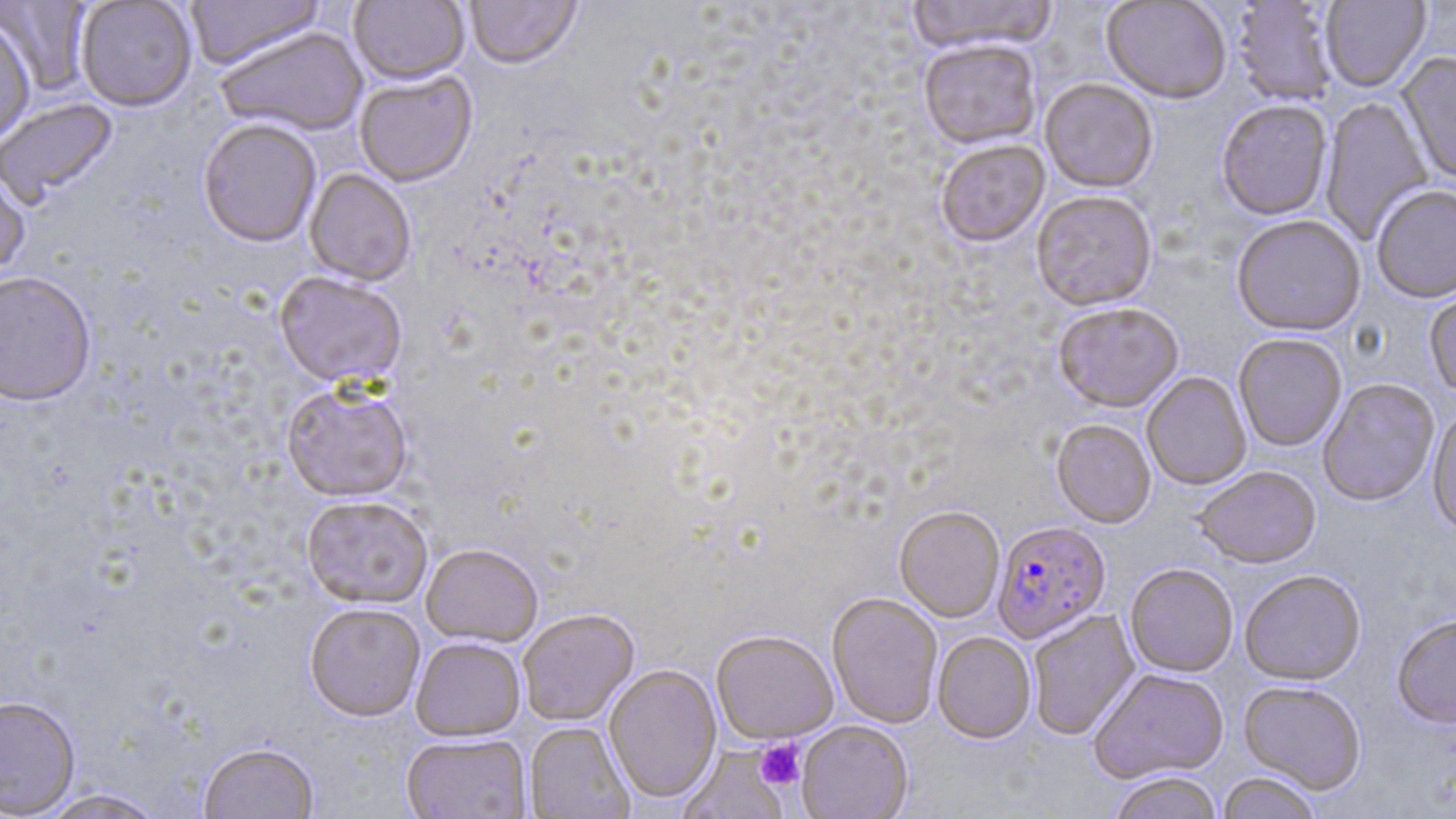
Approximate bounding boxes as (x1,y1)-(x2,y2) corner pairs in pixels. Uninfected red blood cell locations: (185,0)-(326,73), (348,0)-(469,88), (464,0)-(583,73), (905,0)-(1058,57), (1101,0)-(1231,106), (0,1)-(95,96), (75,1)-(197,114), (1231,1)-(1340,107), (1320,1)-(1431,94), (0,20)-(36,146), (215,28)-(368,139), (918,42)-(1042,152), (1396,53)-(1456,185), (354,73)-(478,189), (1039,80)-(1158,195), (1319,96)-(1434,246), (1,99)-(120,209), (1216,101)-(1333,223), (197,121)-(322,251), (935,142)-(1050,250), (0,166)-(31,283), (303,169)-(417,288), (1372,187)-(1456,306), (1032,193)-(1157,314), (1231,217)-(1365,339), (0,274)-(96,410), (273,275)-(407,392), (1424,284)-(1456,401), (1053,305)-(1184,415), (1233,335)-(1347,453), (1142,373)-(1252,491), (1317,379)-(1440,509), (281,386)-(413,505), (1427,409)-(1456,539), (1050,421)-(1156,529), (1194,468)-(1321,571), (301,497)-(432,611), (894,507)-(1005,623), (421,545)-(543,649), (1124,565)-(1238,679), (1240,571)-(1367,688), (826,593)-(943,730), (304,605)-(424,724), (517,610)-(640,727), (1027,610)-(1141,741), (1392,616)-(1456,730), (711,631)-(839,745), (932,632)-(1036,745), (410,639)-(526,742), (604,665)-(722,806), (1089,670)-(1229,785), (1238,682)-(1366,796), (0,697)-(81,818), (796,721)-(913,819), (524,722)-(634,818), (401,735)-(532,819), (199,743)-(321,818), (675,745)-(792,819), (1216,772)-(1323,819), (1108,773)-(1222,819), (36,789)-(168,819). Plasmodium falciparum-infected red blood cell locations: (992,522)-(1111,645). Platelet locations: (755,739)-(805,790). Slide-level diagnosis: Plasmodium falciparum. Image is 1456×819 pixels. Light microscopy. May-Grünwald-Giemsa stain. One field of a larger specimen. 1000x magnification. Thin blood smear.